Classify this cell by malaria status.
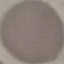
It is uninfected.

{
  "image_type": "automatically extracted cell patch, resized to 64 × 64 pixels",
  "capture": "smartphone through the microscope eyepiece",
  "stain": "Giemsa",
  "preparation": "thin smear"
}